Locate every Plasmodium parasite.
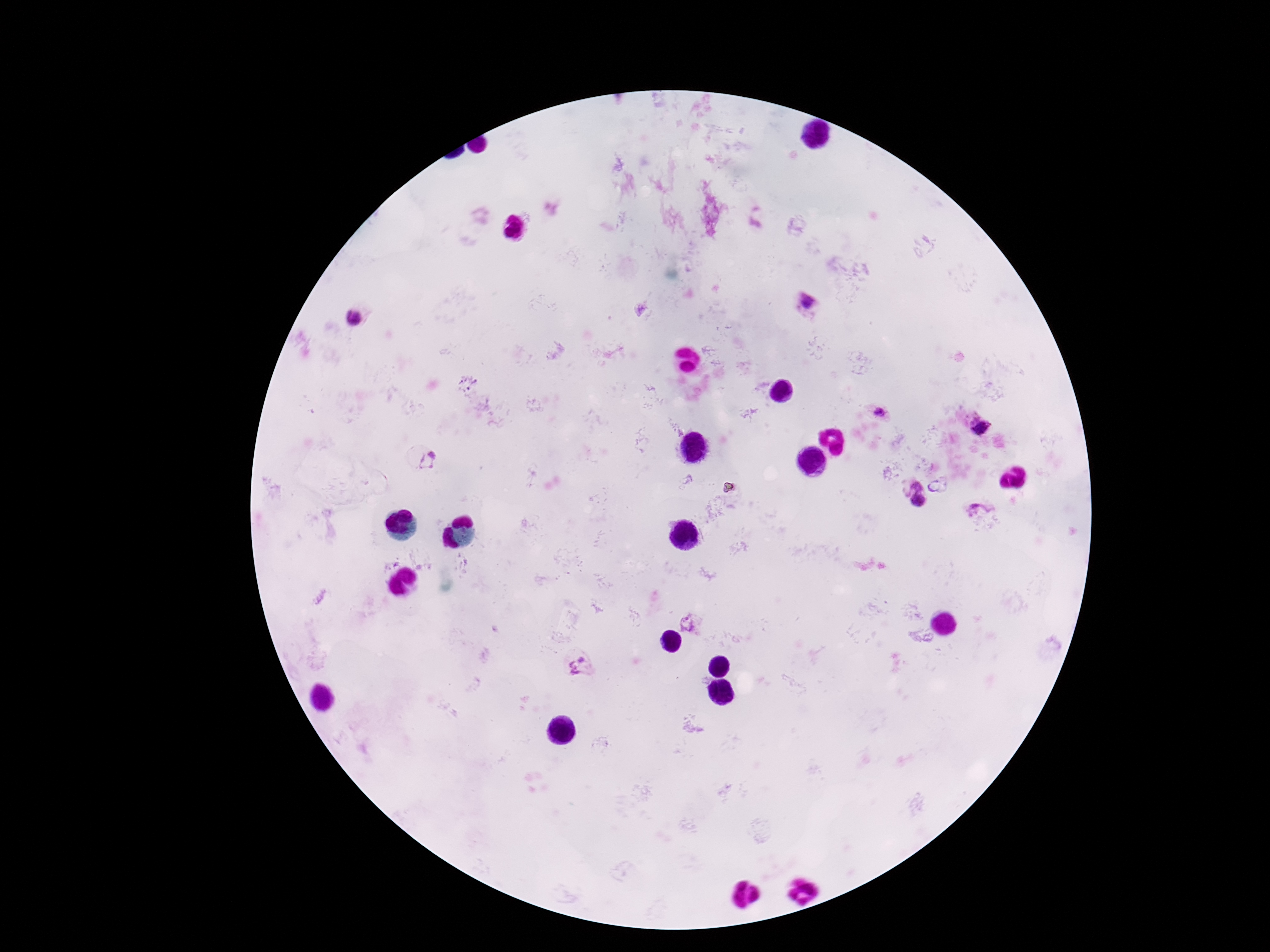
Approximate centers as [x, y] in pixels.
Plasmodium parasites: [805, 301], [352, 318], [878, 412], [980, 427], [430, 463], [918, 486], [933, 486], [918, 502], [979, 511], [689, 623], [580, 668].

capture = smartphone camera through the microscope eyepiece
field of view = single
patient malaria status = positive
magnification = 100x
image size = 1270×952 pixels
preparation = thick blood smear
stain = Giemsa